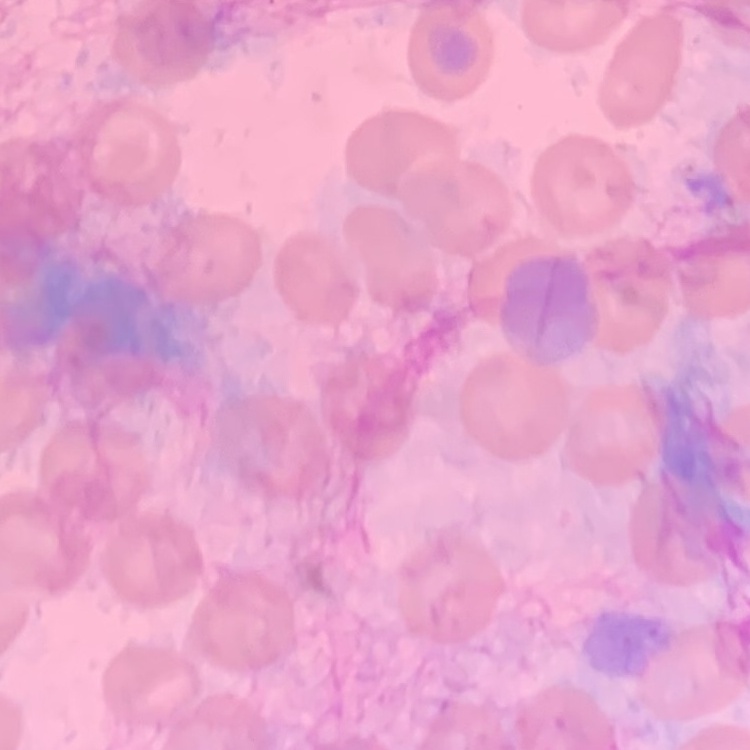
red_blood_cell_morphology: no rouleaux formation
preparation: thin peripheral smear
image_type: one tile cut from a larger photomicrograph
stain: Field's or Giemsa